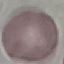

result: no malaria parasites detected
capture: smartphone camera at the microscope eyepiece
stain: Giemsa
image_type: automatically extracted cell patch, resized to 64 × 64 pixels
preparation: thin smear